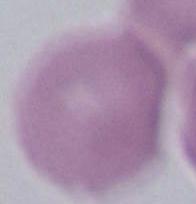
Summary:
  - Magnification: 1000x
  - Modality: photomicrograph
  - Identification: erythrocyte